Report the malaria status of this cell.
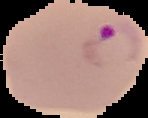

Parasitized.

Summary:
  - Image type: cell region segmented out of the field of view; surrounding area masked to black
  - Image size: 148×118 pixels
  - Preparation: thin blood film